Report the malaria status of this cell.
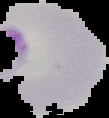

It is parasitized.

Summary:
  - Image size: 109×118 pixels
  - Image type: cell region segmented out of the field of view; surrounding area masked to black
  - Preparation: thin blood smear